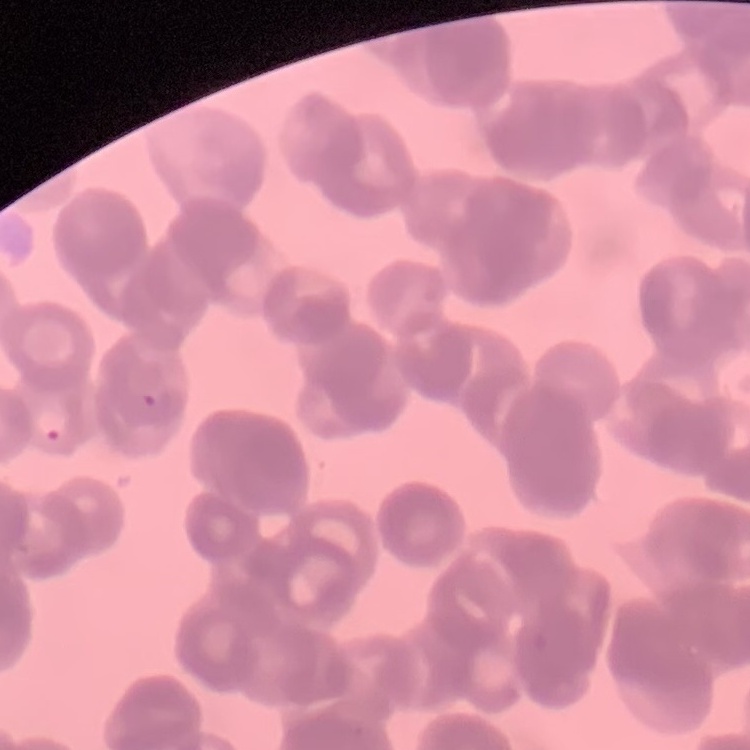

red blood cell morphology = rouleaux formation
preparation = thin peripheral smear
image type = square crop of a larger photomicrograph
stain = Field's or Giemsa